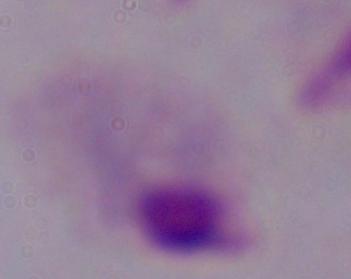

Summary:
  - Identification: trichomonad
  - Modality: micrograph
  - Magnification: 1000x